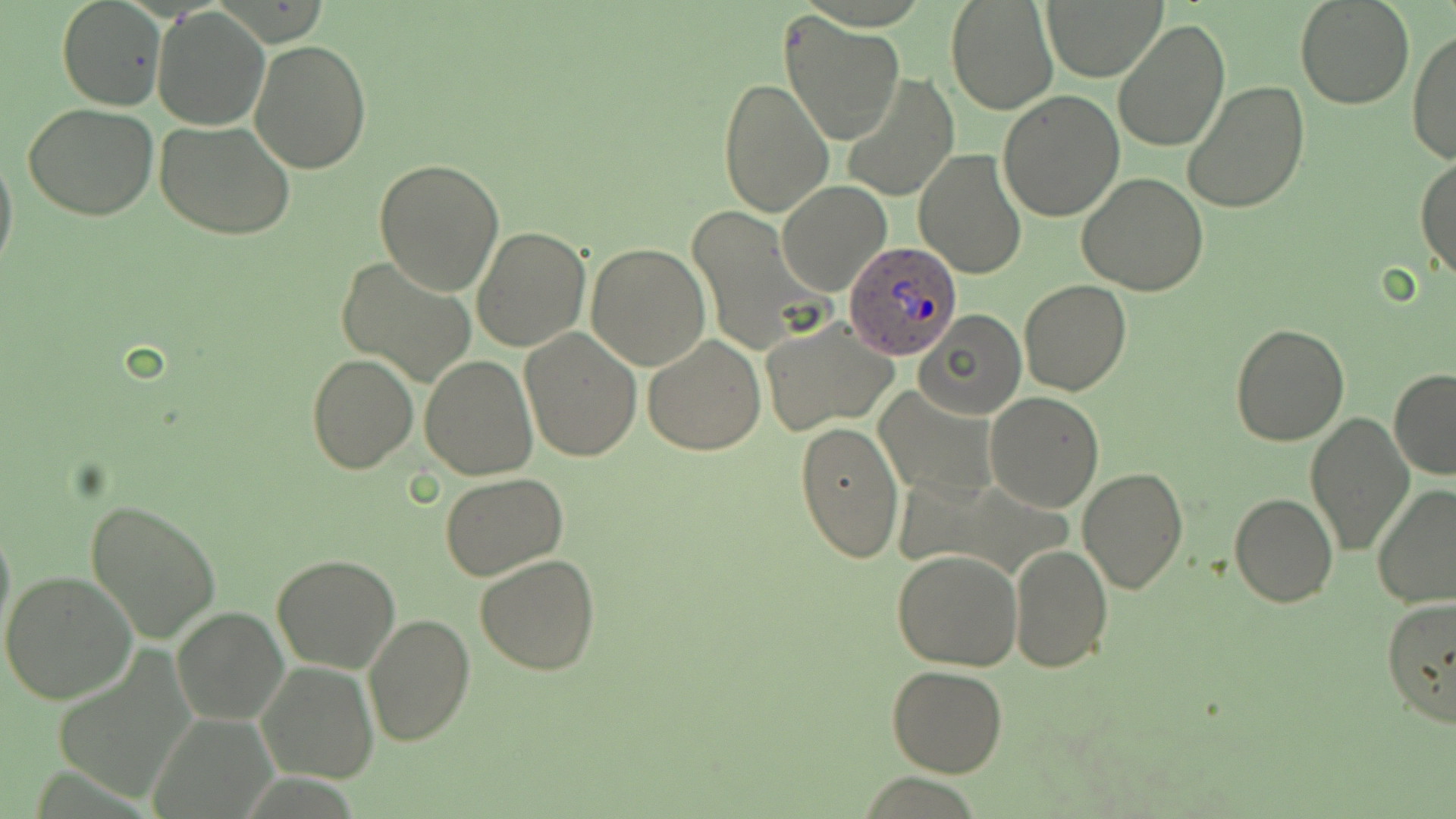
Approximate bounding boxes as (x1, y1, x2, y2) in pixels. Plasmodium ovale-infected red blood cell locations: (845, 238, 963, 362). Uninfected red blood cell locations: (945, 0, 1059, 116), (1044, 0, 1164, 80), (1294, 0, 1416, 111), (59, 1, 166, 111), (151, 7, 271, 131), (780, 12, 905, 147), (1113, 19, 1230, 153), (1409, 30, 1456, 164), (250, 39, 374, 174), (841, 73, 958, 202), (717, 76, 833, 217), (1182, 82, 1311, 213), (997, 91, 1124, 221), (21, 102, 159, 222), (156, 119, 295, 240), (0, 138, 18, 280), (915, 148, 1028, 281), (1415, 153, 1456, 284), (374, 159, 504, 294), (1077, 172, 1208, 296), (776, 181, 891, 297), (686, 203, 826, 354), (471, 225, 591, 353), (587, 243, 710, 370), (337, 256, 478, 389), (1019, 280, 1132, 396), (914, 309, 1026, 420), (760, 320, 898, 435), (1229, 322, 1348, 445), (518, 326, 643, 463), (642, 335, 767, 456), (306, 352, 417, 474), (420, 354, 537, 479), (1389, 369, 1456, 480), (875, 386, 998, 502), (985, 392, 1104, 511), (1304, 411, 1412, 555), (797, 419, 903, 563), (1078, 465, 1188, 594), (440, 472, 567, 581), (1370, 484, 1456, 609), (1228, 492, 1339, 608), (85, 496, 221, 643), (0, 513, 15, 647), (1009, 541, 1113, 672), (893, 550, 1022, 670), (271, 554, 401, 673), (475, 554, 602, 676), (0, 570, 136, 705), (1380, 596, 1456, 728), (171, 606, 288, 726), (206, 614, 363, 746), (363, 614, 475, 747), (256, 661, 379, 784), (885, 665, 1008, 778). Slide-level diagnosis: Plasmodium ovale. One field of a larger specimen. Image is 1456×819 pixels. Light microscopy. May-Grünwald-Giemsa-stained preparation. Thin blood smear. 1000x magnification.